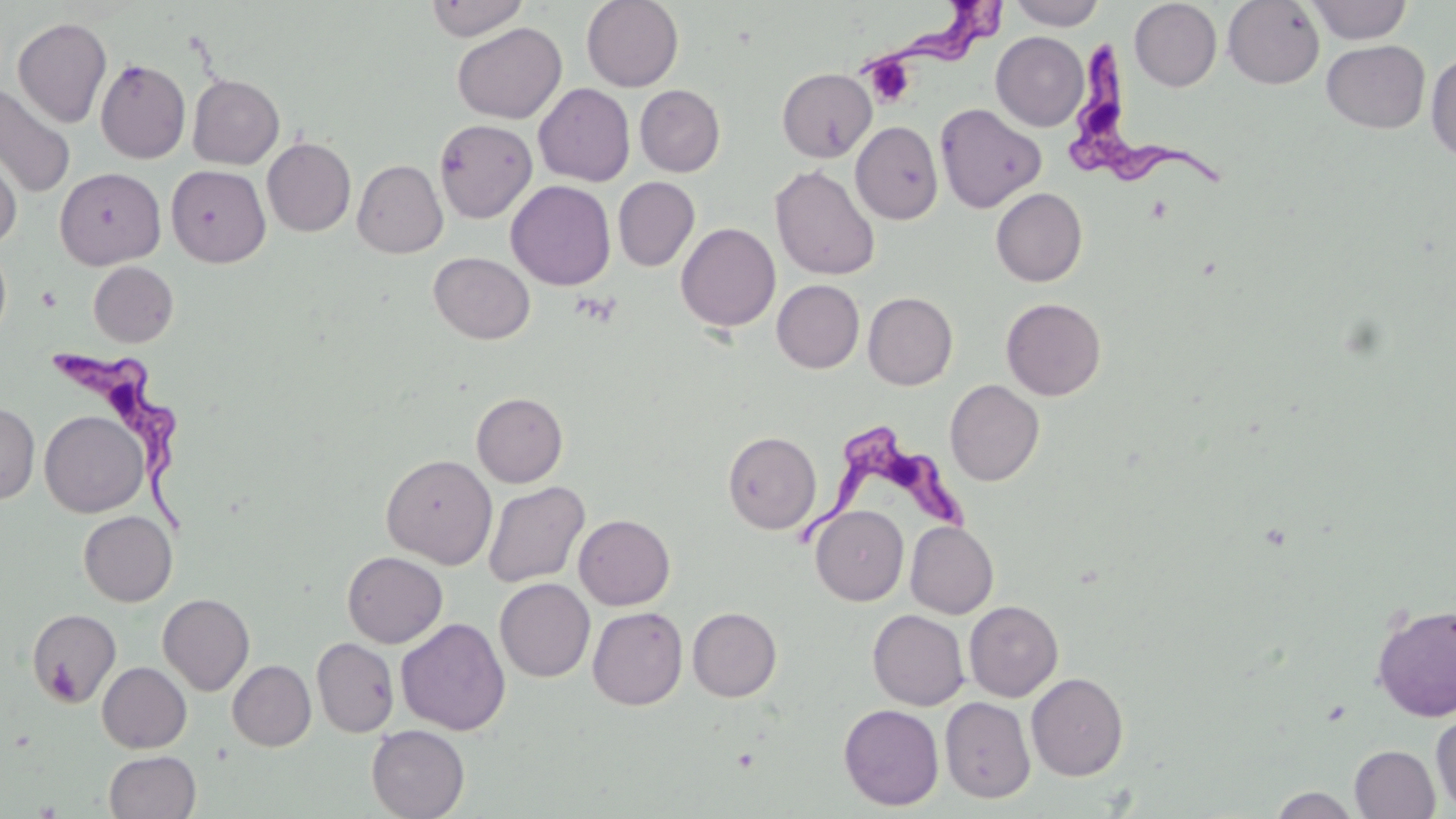
Summary:
  - Coordinate format: approximate bounding boxes as [x1, y1, x2, y2] in pixels
  - Uninfected red blood cell locations: [425, 0, 529, 40], [581, 0, 684, 91], [1007, 0, 1106, 29], [1129, 0, 1222, 91], [1223, 0, 1325, 88], [1306, 0, 1412, 44], [13, 17, 112, 128], [451, 22, 567, 123], [991, 31, 1088, 131], [1321, 40, 1431, 133], [1426, 50, 1456, 161], [95, 59, 191, 163], [777, 68, 876, 162], [187, 74, 284, 169], [534, 83, 635, 186], [635, 84, 725, 177], [0, 85, 75, 198], [935, 103, 1047, 213], [435, 119, 537, 222], [851, 121, 943, 224], [262, 137, 356, 237], [0, 147, 22, 248], [351, 159, 448, 258], [166, 164, 270, 267], [770, 165, 881, 281], [54, 168, 165, 268], [613, 177, 700, 271], [506, 180, 616, 291], [991, 188, 1087, 286], [998, 190, 1095, 400], [676, 222, 781, 331], [0, 242, 11, 345], [429, 252, 535, 344], [89, 261, 179, 347], [772, 279, 864, 373], [863, 292, 957, 390], [1001, 297, 1106, 400], [945, 379, 1044, 486], [471, 392, 568, 487], [0, 402, 39, 505], [39, 410, 149, 517], [722, 431, 821, 534], [381, 453, 498, 568], [483, 481, 590, 588], [810, 505, 908, 605], [78, 511, 177, 606], [574, 514, 675, 610], [905, 521, 999, 618], [342, 551, 448, 648], [494, 578, 595, 682], [158, 593, 255, 695], [964, 600, 1063, 701], [1372, 602, 1456, 722], [587, 607, 688, 710], [688, 607, 782, 701], [26, 608, 121, 708], [868, 609, 969, 710], [395, 617, 510, 736], [312, 638, 399, 737], [228, 660, 316, 751], [97, 662, 191, 753], [1026, 672, 1129, 780], [940, 696, 1036, 804], [839, 704, 944, 811], [1431, 711, 1456, 813], [366, 725, 470, 819], [1350, 745, 1440, 819], [103, 750, 200, 818], [1268, 787, 1363, 818]
  - Trypanosoma brucei locations: [855, 2, 1007, 86], [1064, 39, 1221, 192], [52, 346, 202, 534], [796, 423, 980, 554]
  - Platelet locations: [863, 53, 918, 109]
  - Slide-level diagnosis: Trypanosoma brucei
  - Field of view: single
  - Preparation: thin blood smear
  - Stain: May-Grünwald-Giemsa
  - Magnification: 1000x
  - Modality: light microscopy
  - Image size: 1456×819 pixels